Report the malaria status of this cell.
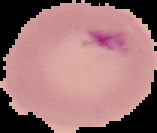

Parasitized.

From a thin blood smear. Image is 157×133 pixels. Segmented cell region on a black background.